Assess this cell for malaria.
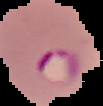

It is parasitized.

From a thin blood film. Segmented cell region on a black background. Image is 103×106 pixels.